Comment on the morphology of the erythrocytes.
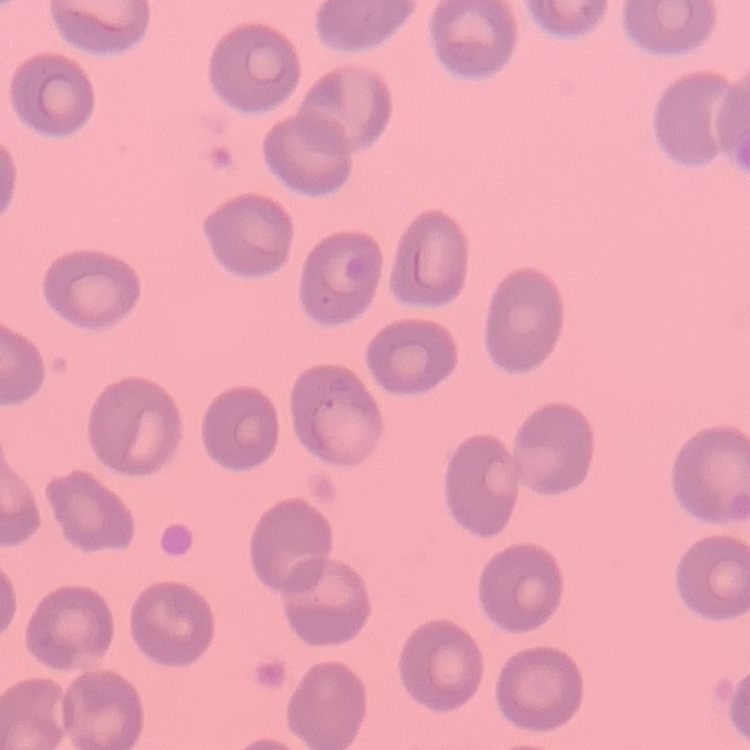

They show no rouleaux formation.

preparation: thin blood smear
image_type: square crop of a larger photomicrograph
stain: Field's or Giemsa